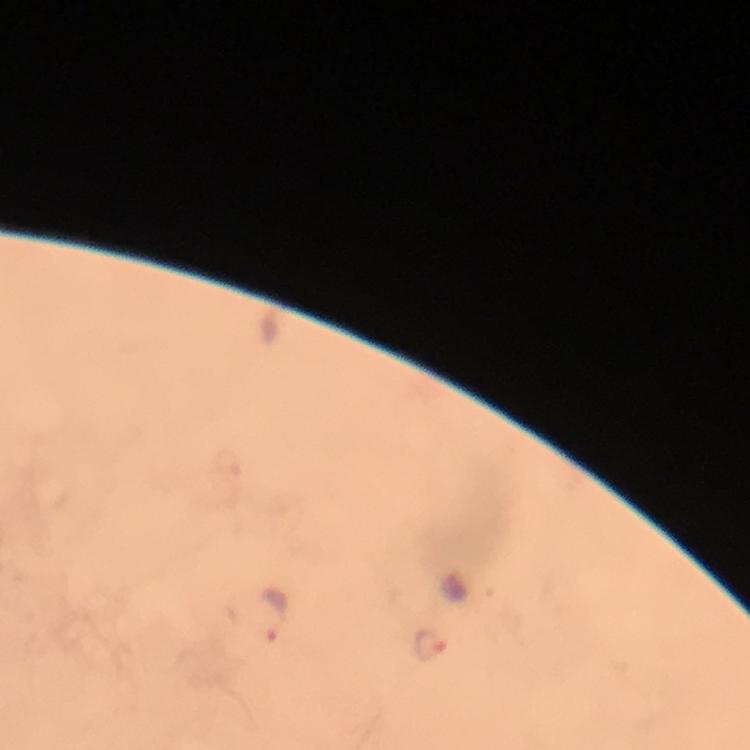

Approximate centers as (x, y) in pixels.
Summary:
  - Malaria parasite locations: (275, 615), (430, 644)
  - Stain: Giemsa
  - Capture: smartphone mounted on the microscope
  - Preparation: thick smear
  - Image size: 750×750 pixels
  - Context: from a malaria diagnostic workup
  - Magnification: 100x
  - Immersion oil: used
  - Cropped from: one field of view